Assess the morphology of the erythrocytes.
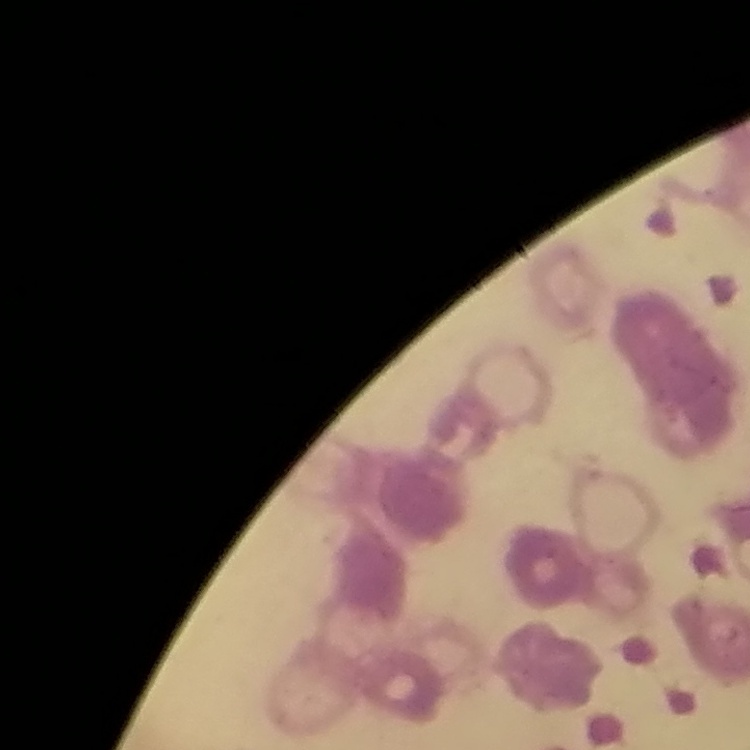

Rouleaux formation.

Summary:
  - Preparation: thin peripheral smear
  - Image type: square crop of a larger photomicrograph
  - Stain: Field's or Giemsa